Assess this cell for malaria.
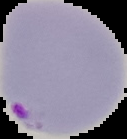
It is parasitized.

{
  "preparation": "thin blood film",
  "image_size": "127×139 pixels",
  "image_type": "cell region segmented out of the field of view; surrounding area masked to black"
}